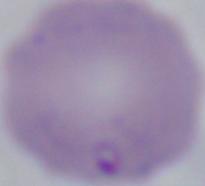

Summary:
  - Identification: Babesia
  - Modality: micrograph
  - Magnification: 1000x